Comment on the morphology of the red blood cells.
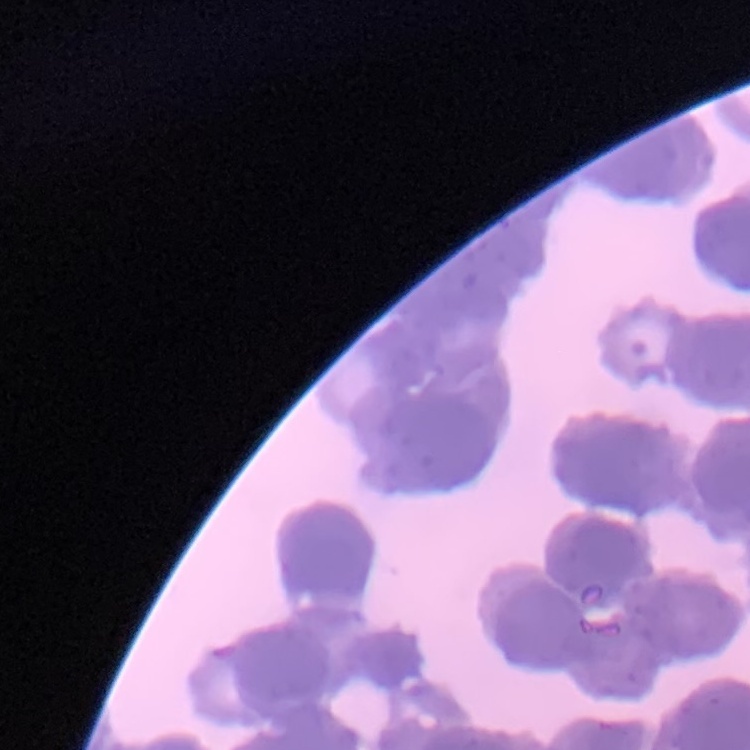

They show rouleaux formation.

Field's or Giemsa stain. One tile cut from a larger photomicrograph. Thin blood smear.